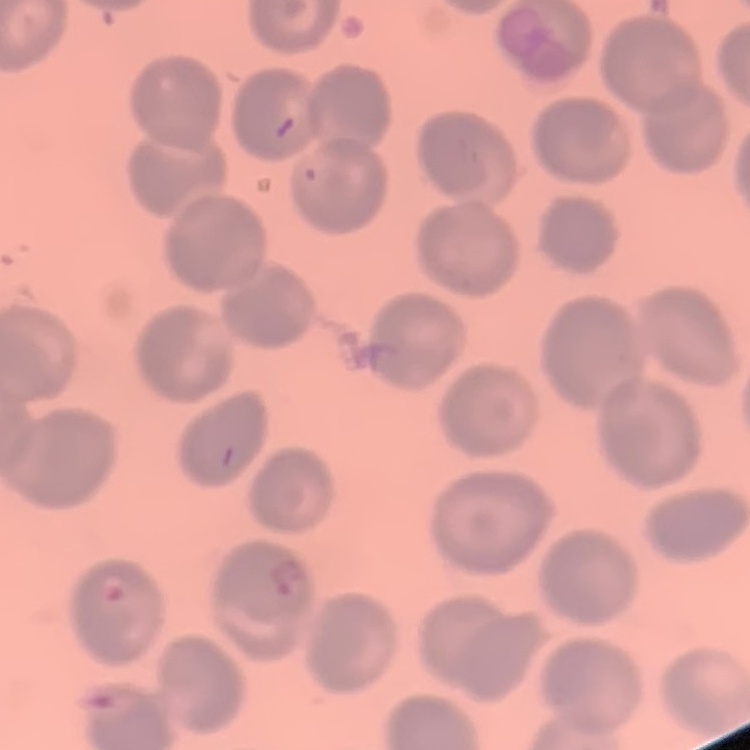 The red blood cells exhibit no rouleaux formation. Thin blood film. One tile cut from a larger photomicrograph. Stained with either Field's or Giemsa.